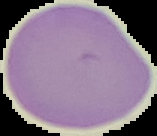
Image is 157×136 pixels. From a thin blood film. Malaria status: uninfected. Cell region segmented out of the field of view; the surrounding area is masked to black.